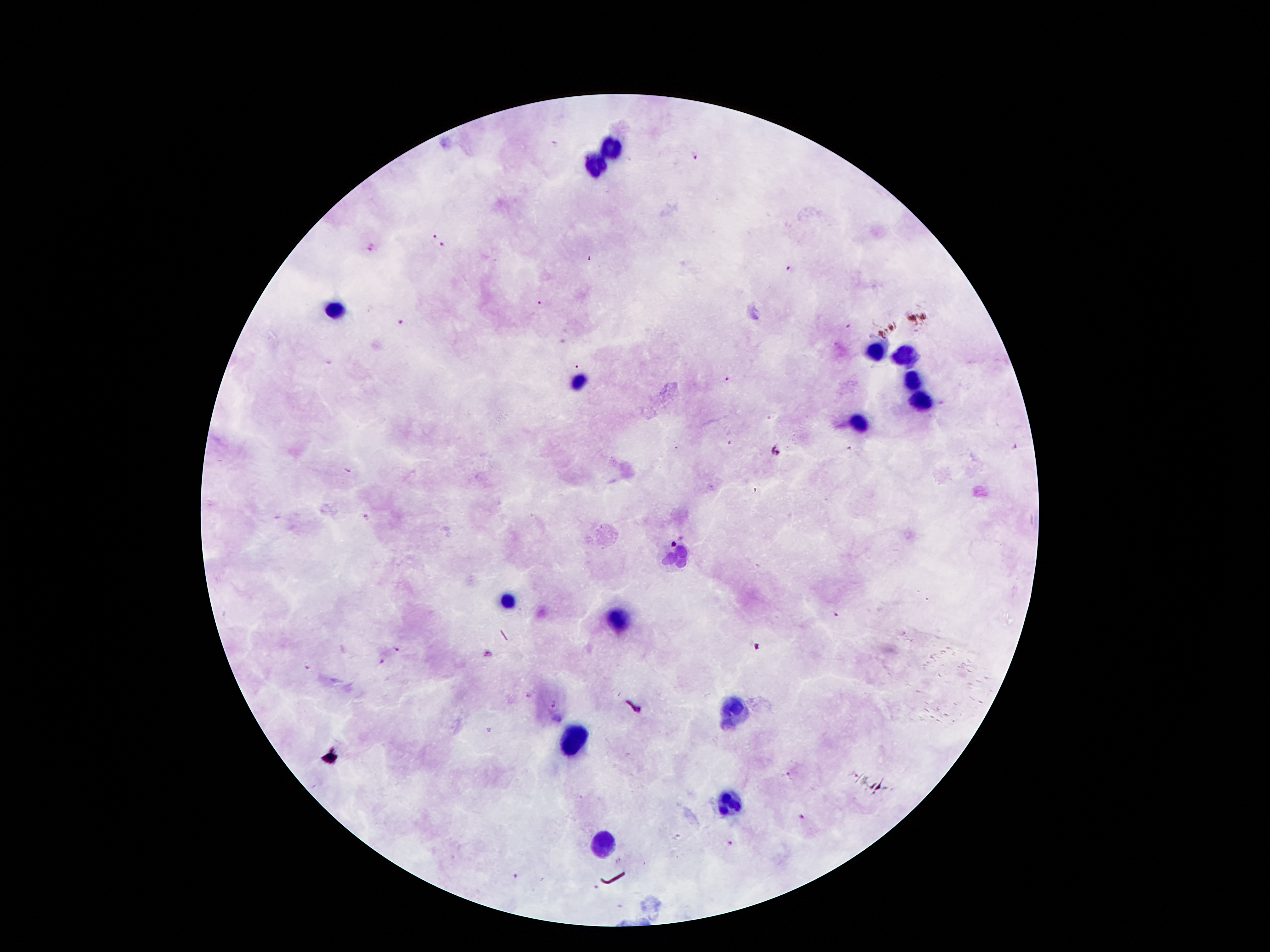 Approximate centers as [x, y] in pixels. Leukocyte locations: [610, 149], [596, 164], [333, 310], [876, 351], [905, 357], [574, 382], [912, 383], [923, 398], [860, 423], [677, 559], [506, 600], [621, 622], [730, 712], [575, 737], [728, 798], [603, 846]. Malaria parasite locations: [553, 145], [694, 156], [433, 233], [373, 246], [443, 246], [790, 269], [540, 303], [400, 322], [848, 326], [330, 362], [578, 368], [729, 379], [730, 443], [1014, 448], [850, 449], [775, 451], [349, 471], [756, 491], [366, 516], [837, 615], [397, 648], [488, 654], [382, 661], [309, 666], [528, 695], [554, 704], [490, 730], [790, 775], [802, 817], [729, 844], [518, 876]. Thick peripheral-blood smear. Image is 1270×952 pixels. One field from this slide. 100x magnification. Photographed through the microscope eyepiece with a smartphone camera. Giemsa-stained preparation. Patient malaria status: infected with Plasmodium falciparum.